Assess this cell for malaria.
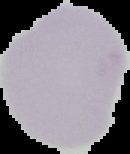
Uninfected.

image size = 130×154 pixels
preparation = thin blood film
image type = segmented cell region with the area outside set to black